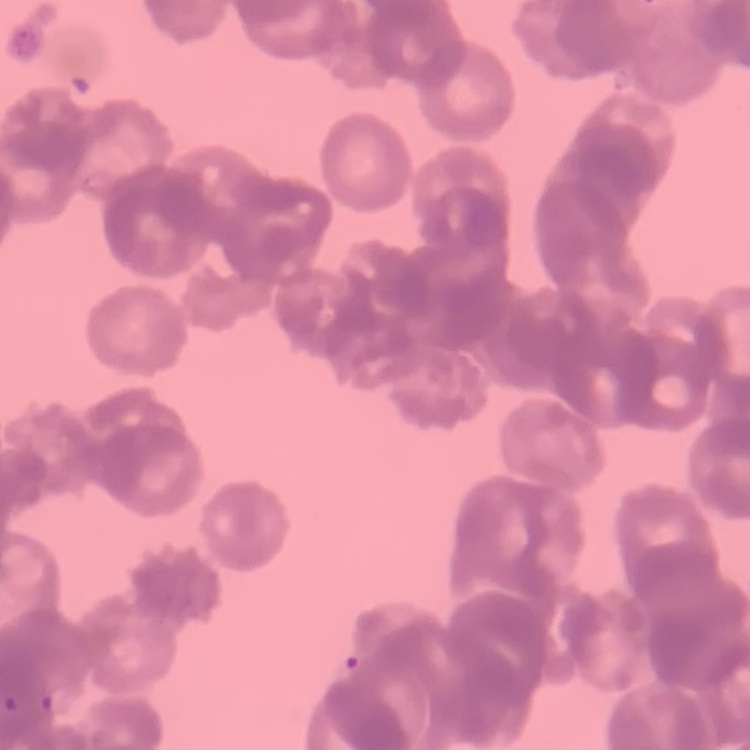
red blood cell morphology = rouleaux formation
stain = Field's or Giemsa
preparation = thin peripheral smear
image type = one tile cut from a larger photomicrograph